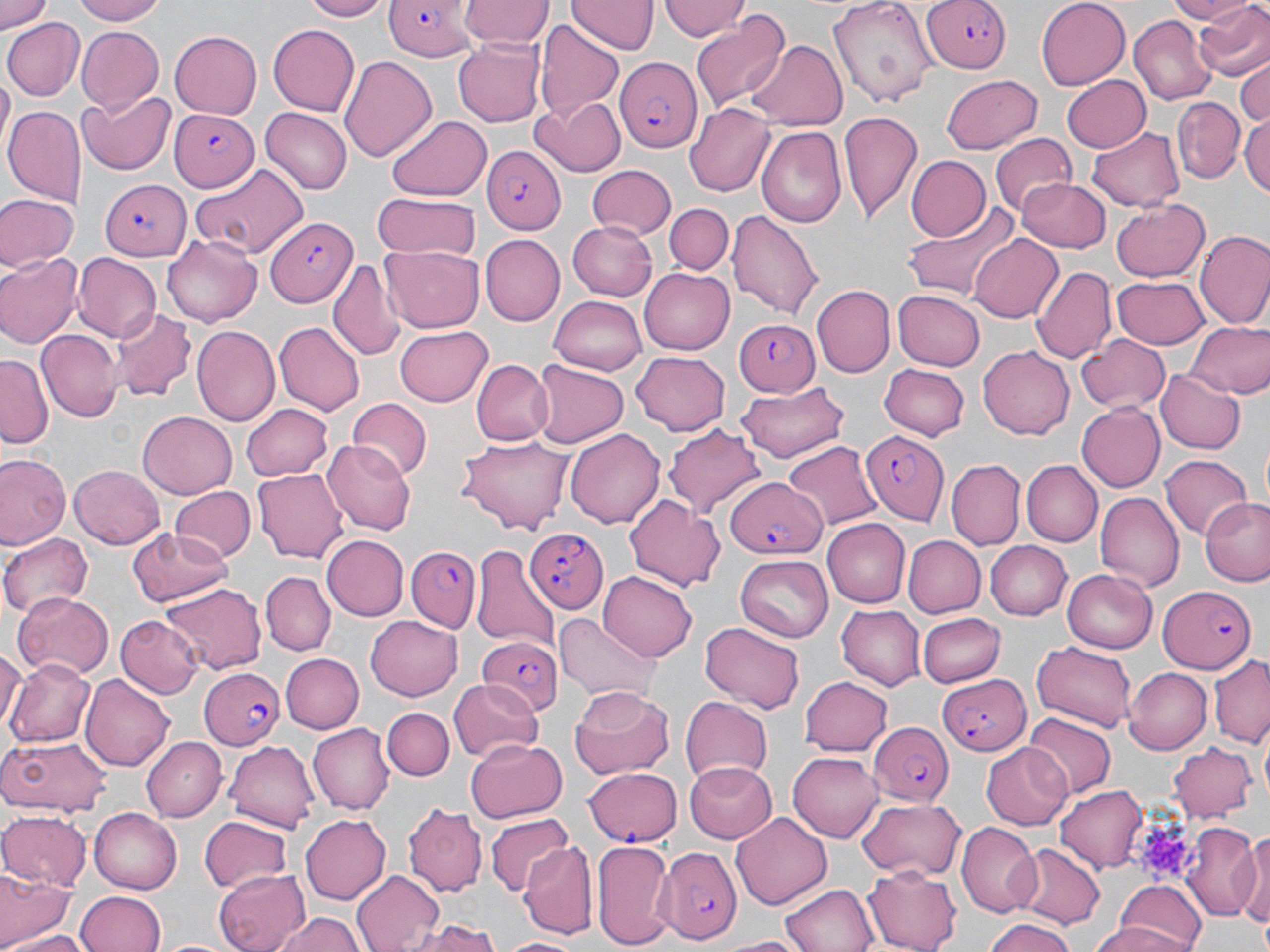
Approximate bounding boxes as (x1, y1, x2, y2) in pixels. Plasmodium falciparum-infected red blood cell locations: (923, 0, 1014, 76), (384, 1, 480, 60), (615, 57, 702, 154), (169, 109, 259, 191), (483, 147, 566, 234), (99, 178, 189, 261), (265, 218, 355, 307), (731, 318, 822, 396), (862, 430, 949, 524), (724, 477, 823, 559), (525, 526, 607, 616), (407, 545, 483, 636), (1157, 583, 1258, 674), (474, 635, 562, 718), (198, 667, 286, 750), (936, 672, 1032, 759), (867, 722, 955, 807), (582, 766, 682, 846), (662, 847, 741, 943). Platelet locations: (1131, 817, 1199, 880). Uninfected red blood cell locations: (0, 0, 55, 35), (69, 0, 174, 24), (298, 0, 390, 21), (460, 0, 551, 48), (568, 0, 656, 55), (661, 0, 750, 42), (829, 0, 937, 108), (1036, 0, 1131, 90), (1165, 0, 1255, 23), (1194, 0, 1270, 84), (690, 11, 791, 110), (1128, 15, 1215, 105), (1, 18, 82, 101), (534, 22, 625, 121), (267, 24, 360, 114), (76, 27, 165, 112), (168, 30, 262, 120), (453, 36, 546, 126), (747, 40, 848, 131), (339, 54, 437, 164), (1234, 60, 1270, 129), (2, 72, 12, 151), (941, 73, 1041, 153), (1061, 76, 1150, 151), (75, 90, 178, 176), (530, 96, 625, 176), (1173, 97, 1244, 182), (687, 102, 779, 196), (4, 106, 85, 204), (261, 107, 352, 194), (839, 111, 925, 224), (1240, 113, 1270, 196), (387, 114, 493, 202), (756, 125, 846, 228), (1088, 127, 1184, 210), (989, 132, 1078, 216), (904, 155, 990, 242), (189, 162, 306, 259), (586, 165, 675, 240), (1019, 176, 1112, 253), (373, 193, 479, 260), (0, 194, 77, 270), (1111, 200, 1213, 282), (664, 203, 733, 279), (901, 204, 1020, 304), (728, 208, 822, 322), (566, 219, 658, 301), (1195, 231, 1270, 332), (163, 233, 263, 326), (968, 233, 1063, 325), (479, 235, 564, 326), (381, 247, 485, 332), (0, 251, 83, 348), (73, 253, 160, 342), (329, 256, 404, 362), (1031, 266, 1116, 367), (639, 267, 734, 355), (1111, 274, 1210, 349), (812, 286, 894, 378), (893, 290, 985, 370), (549, 294, 648, 374), (110, 308, 194, 399), (1186, 321, 1270, 398), (275, 323, 363, 414), (393, 325, 494, 405), (192, 326, 279, 427), (36, 330, 120, 423), (1076, 332, 1172, 413), (977, 346, 1073, 439), (631, 352, 731, 434), (0, 355, 52, 447), (471, 360, 554, 447), (531, 361, 627, 450), (880, 363, 972, 439), (1156, 368, 1245, 454), (734, 382, 852, 462), (344, 398, 431, 482), (1077, 402, 1166, 492), (241, 403, 336, 481), (138, 411, 237, 498), (664, 422, 765, 517), (566, 428, 665, 527), (457, 435, 574, 536), (325, 439, 415, 534), (783, 440, 883, 531), (0, 452, 70, 551), (1161, 453, 1251, 541), (948, 459, 1024, 549), (1021, 460, 1100, 547), (69, 464, 168, 549), (254, 467, 349, 565), (168, 485, 256, 563), (622, 492, 727, 592), (1095, 492, 1182, 588), (1200, 497, 1270, 586), (821, 519, 909, 607), (126, 527, 234, 609), (0, 532, 95, 618), (323, 534, 409, 620), (901, 535, 986, 618), (983, 540, 1071, 620), (472, 544, 559, 654), (736, 555, 834, 641), (1060, 569, 1156, 655), (599, 571, 695, 662), (261, 572, 334, 655), (160, 580, 265, 675), (12, 589, 113, 679), (836, 605, 926, 690), (116, 612, 206, 698), (365, 613, 464, 699), (555, 613, 659, 702), (916, 613, 1004, 687), (698, 619, 806, 713), (1030, 640, 1137, 732), (0, 649, 22, 733), (278, 653, 364, 734), (1208, 656, 1269, 747), (6, 659, 97, 747), (1123, 666, 1212, 752), (82, 673, 177, 771), (450, 677, 544, 761), (800, 677, 894, 756), (568, 685, 678, 780), (679, 695, 772, 783), (382, 705, 455, 780), (1025, 713, 1116, 797), (311, 723, 396, 815), (0, 733, 113, 815), (142, 738, 225, 819), (467, 738, 568, 823), (226, 740, 323, 831), (980, 741, 1075, 830), (1169, 742, 1258, 821), (789, 751, 884, 840), (681, 761, 777, 844), (1054, 784, 1149, 873), (856, 798, 967, 881), (405, 802, 486, 899), (88, 808, 181, 894), (0, 811, 90, 892), (732, 812, 833, 910), (299, 813, 393, 903), (487, 813, 573, 897), (199, 816, 295, 895), (955, 823, 1039, 916), (1181, 824, 1261, 917), (1240, 825, 1269, 938), (591, 838, 674, 950), (522, 841, 597, 937), (1014, 843, 1104, 930), (0, 866, 73, 950), (350, 867, 444, 952), (863, 867, 963, 951), (214, 868, 310, 952), (1114, 881, 1208, 952), (780, 882, 881, 952), (73, 892, 165, 952), (274, 911, 365, 952), (409, 917, 499, 952), (983, 917, 1079, 952), (1082, 923, 1194, 952), (6, 932, 92, 952), (712, 934, 809, 952), (500, 935, 581, 951), (154, 937, 238, 952). Slide-level diagnosis: Plasmodium falciparum. Thin blood smear. Optical microscopy. May-Grünwald-Giemsa stain. Image is 1270×952 pixels. 1000x magnification. One field of a larger specimen.